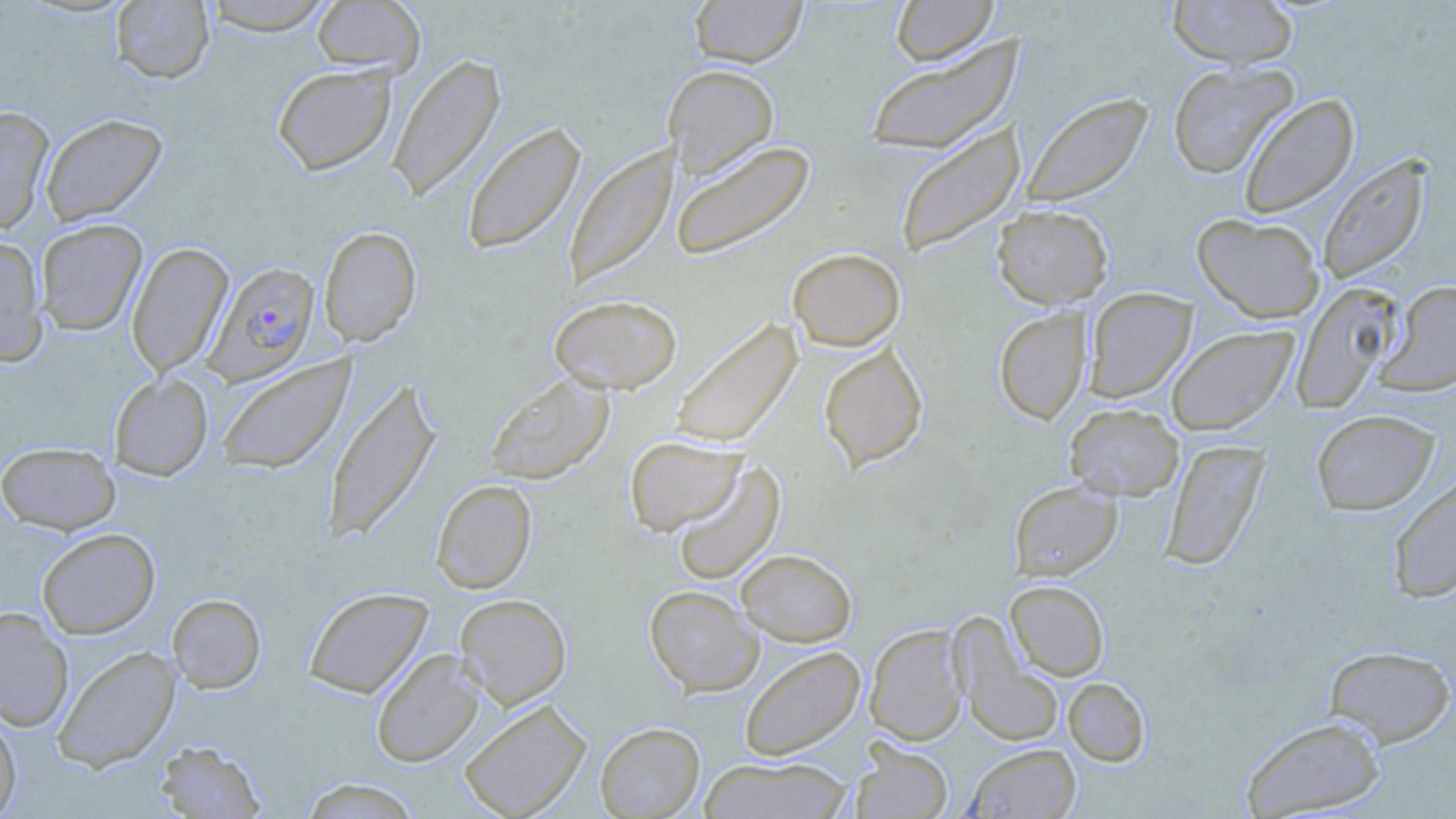
Plasmodium falciparum-infected red blood cell locations = approximate bounding boxes as (x1, y1, x2, y2) in pixels: (205, 261, 320, 385)
slide-level diagnosis = Plasmodium falciparum
field of view = single
preparation = thin blood smear
image size = 1456×819 pixels
modality = optical microscopy
uninfected red blood cell locations = approximate bounding boxes as (x1, y1, x2, y2) in pixels: (200, 0, 338, 35), (311, 0, 425, 76), (689, 0, 808, 68), (890, 0, 998, 66), (1167, 0, 1299, 69), (110, 1, 214, 84), (863, 37, 1025, 156), (387, 53, 506, 202), (1167, 61, 1299, 179), (272, 63, 396, 175), (663, 64, 779, 179), (1021, 91, 1154, 209), (1238, 93, 1360, 219), (0, 105, 55, 234), (40, 113, 167, 226), (461, 122, 585, 255), (894, 122, 1025, 259), (669, 139, 817, 262), (564, 144, 676, 289), (1316, 155, 1432, 284), (992, 204, 1113, 309), (1191, 213, 1325, 323), (35, 218, 147, 335), (318, 226, 421, 346), (0, 234, 48, 364), (126, 242, 234, 377), (787, 248, 905, 351), (1376, 281, 1456, 398), (1291, 282, 1402, 412), (1084, 287, 1197, 403), (549, 294, 683, 394), (993, 307, 1092, 425), (670, 318, 803, 450), (1166, 325, 1299, 436), (818, 343, 928, 471), (216, 354, 355, 474), (109, 372, 213, 480), (485, 373, 614, 485), (323, 379, 440, 543), (1064, 403, 1183, 501), (1311, 409, 1439, 515), (624, 435, 745, 536), (1161, 439, 1270, 571), (0, 441, 121, 534), (671, 461, 784, 586), (1387, 471, 1456, 604), (431, 479, 537, 594), (1009, 481, 1122, 581), (37, 527, 160, 639), (736, 549, 856, 646), (1005, 580, 1109, 681), (644, 585, 764, 696), (303, 587, 433, 699), (167, 593, 266, 693), (455, 594, 572, 709), (0, 607, 73, 731), (953, 622, 1064, 748), (864, 624, 967, 745), (52, 645, 181, 772), (1324, 645, 1455, 747), (739, 646, 865, 761), (371, 649, 485, 768), (1063, 677, 1150, 767), (459, 699, 591, 819), (0, 711, 21, 818), (1241, 715, 1388, 818), (594, 722, 704, 818), (155, 740, 265, 818), (850, 742, 953, 818), (964, 743, 1081, 818), (699, 755, 854, 818), (299, 777, 422, 818)
stain = May-Grünwald-Giemsa
magnification = 1000x